Identify the parasite.
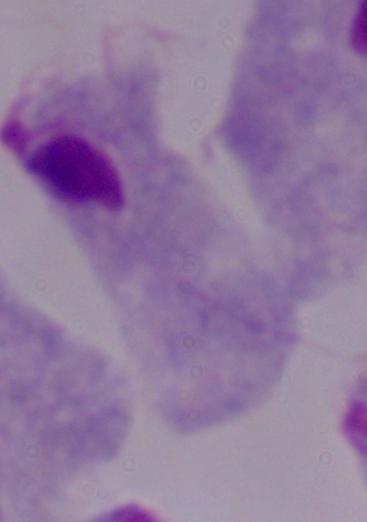

A trichomonad.

Summary:
  - Modality: micrograph
  - Magnification: 1000x